Give the position of every Plasmodium falciparum parasite, noting its life-cycle stage.
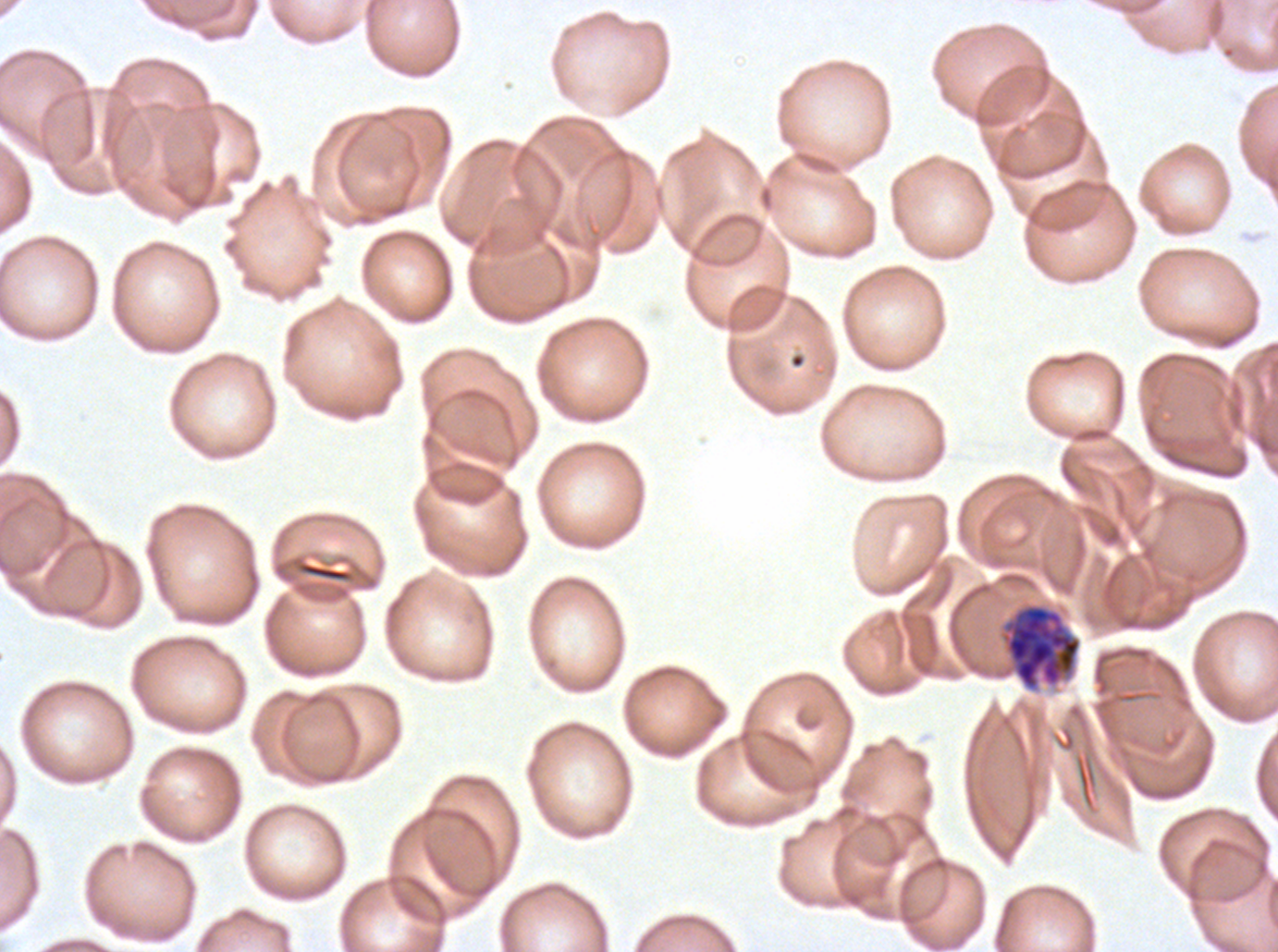
Approximate bounding boxes as [x1, y1, x2, y2] in pixels.
Late schizonts: [999, 602, 1083, 693].
No rings, late-ring/early-trophozoite forms, mid trophozoites, late trophozoites, early schizonts, segmenters, or gametocytes observed.

{
  "stain": "Giemsa",
  "specimen": "ex-vivo Plasmodium falciparum culture from a patient in The Gambia, grown for 24 to 48 hours",
  "preparation": "thin blood smear",
  "image_size": "1278×952 pixels",
  "field_of_view": "sub-image separated from a larger composite"
}